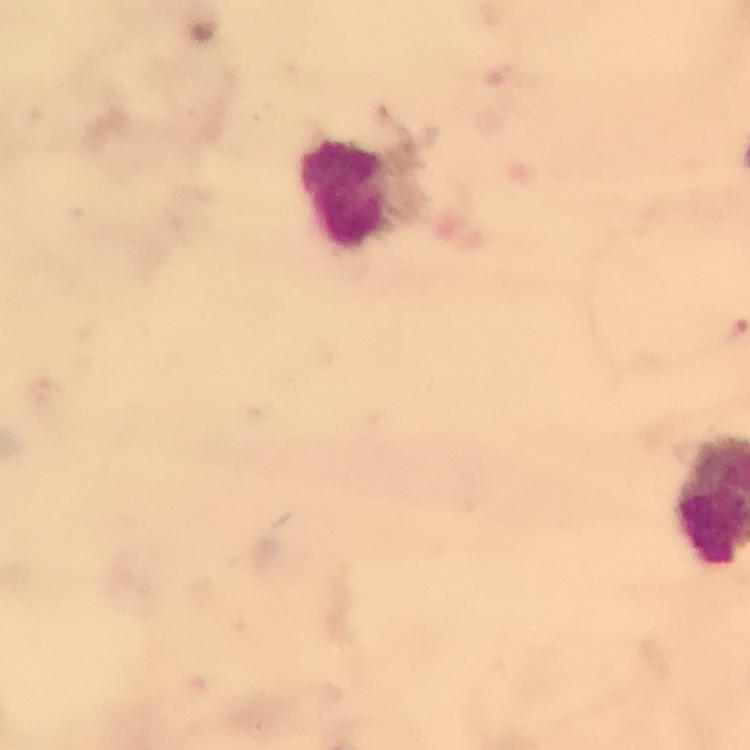
Approximate centers as [x, y] in pixels.
Summary:
  - Leukocyte locations: [345, 195]
  - Magnification: 100x
  - Malaria parasites: none detected
  - Capture: smartphone photograph through a microscope
  - Image size: 750×750 pixels
  - Context: from a diagnostic examination for malaria
  - Stain: Giemsa
  - Preparation: thick blood film
  - Cropped from: one field of view
  - Immersion oil: used